Assess this cell for malaria.
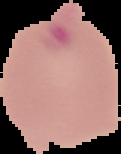
Parasitized.

Summary:
  - Image size: 121×154 pixels
  - Preparation: thin blood film
  - Image type: segmented cell region with the area outside set to black